Evaluate for Plasmodium parasites.
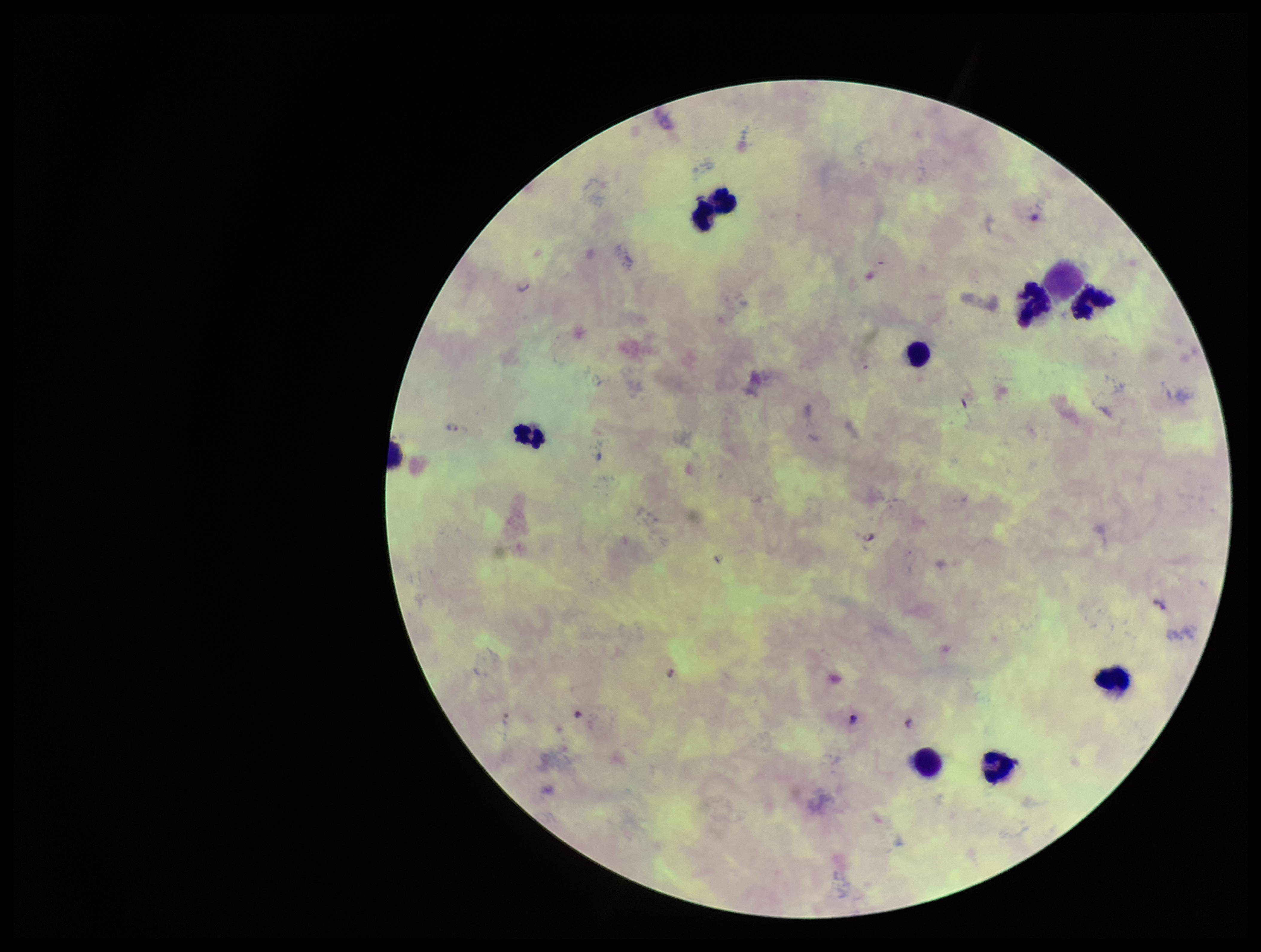

Seen.

Species reported for this patient: Plasmodium falciparum. Image is 1261×952 pixels. Preparation: thick blood smear. Giemsa stain. Parasite count: 1. Patient malaria status: infected. Smartphone photograph taken through the eyepiece of a microscope. Leukocyte count: 8. One field from this slide.